Comment on the morphology of the red blood cells.
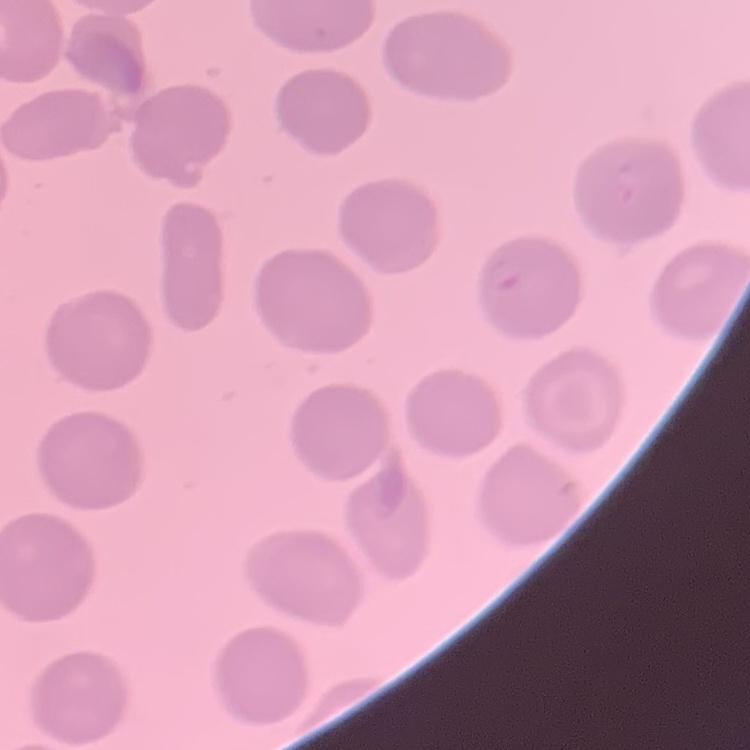
No rouleaux formation.

Square crop of a larger photomicrograph. Stained with either Field's or Giemsa. Thin blood smear.